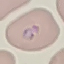

Result: malaria parasites identified. Thin smear of blood. Acquired by smartphone through the microscope eyepiece. Automatically extracted cell patch, resized to 64 × 64 pixels. Giemsa stain.